Assess this cell for malaria.
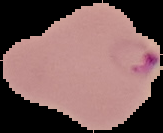
It is parasitized.

Segmented cell region on a black background. Image is 163×133 pixels. From a thin blood film.